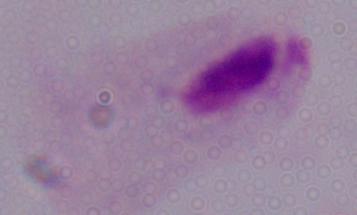
Photomicrograph. A trichomonad is shown. Captured at 1000x magnification.